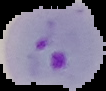
From a thin blood smear. Result: Plasmodium parasites detected. Image is 106×91 pixels. Cell region segmented out of the field of view; the surrounding area is masked to black.